Classify this cell by malaria status.
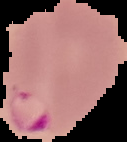

Parasitized.

Image is 127×142 pixels. Segmented cell region on a black background. From a thin blood film.